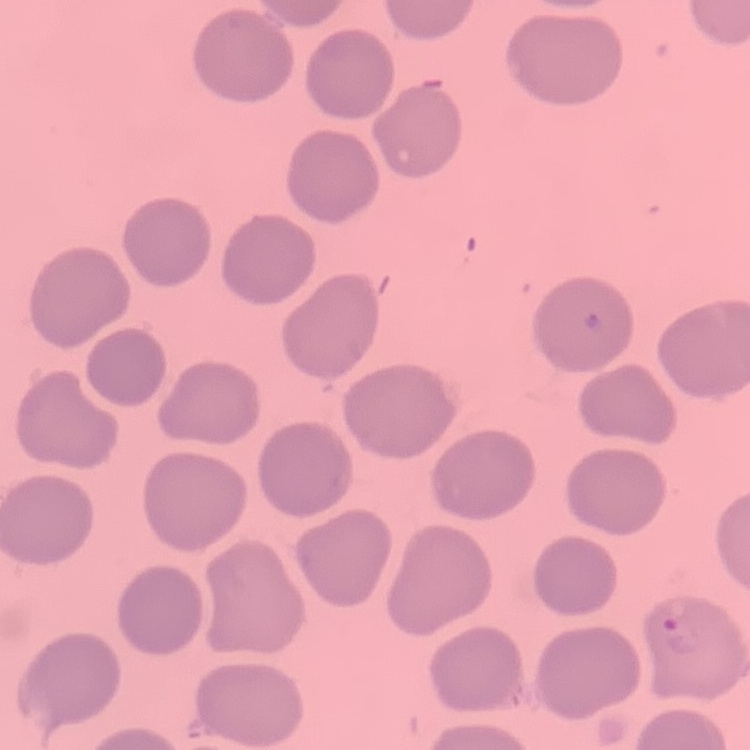

Summary:
  - Red blood cell morphology: no rouleaux formation
  - Stain: Field's or Giemsa
  - Preparation: thin blood smear
  - Image type: square crop of a larger photomicrograph